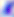

Toxoplasma gondii is shown. Photomicrograph. Captured at 400x magnification.